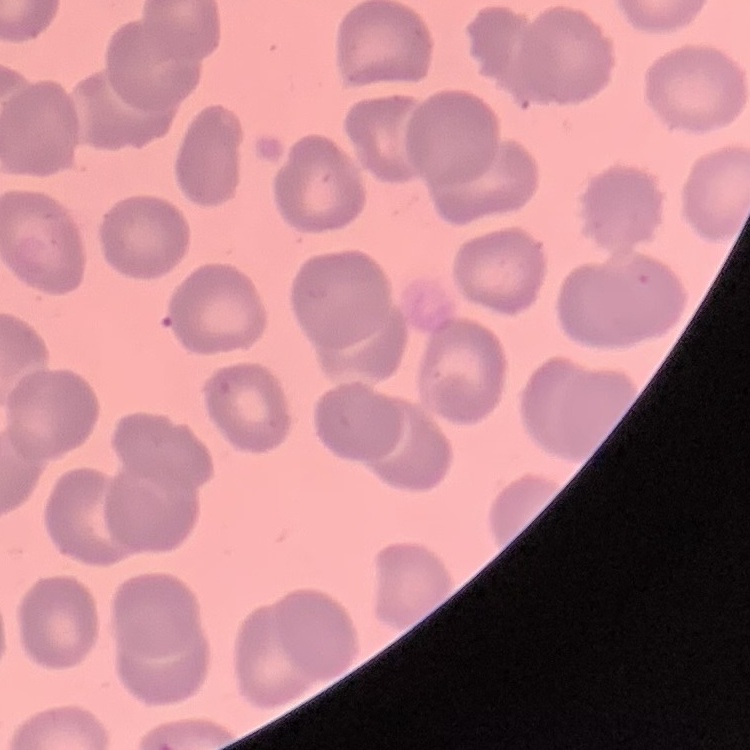 The red blood cells show no rouleaux formation. Thin peripheral smear. Square crop of a larger photomicrograph. Field's or Giemsa stain.